Assess this cell for malaria.
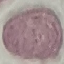
Uninfected.

Summary:
  - Stain: Giemsa
  - Capture: smartphone through the microscope eyepiece
  - Image type: cell patch, automatically extracted from a larger field of view and resized to 64 × 64 pixels
  - Preparation: thin blood smear